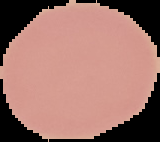

malaria status = uninfected
preparation = thin blood film
image type = cell region segmented out of the field of view; surrounding area masked to black
image size = 160×142 pixels